Evaluate for Plasmodium parasites.
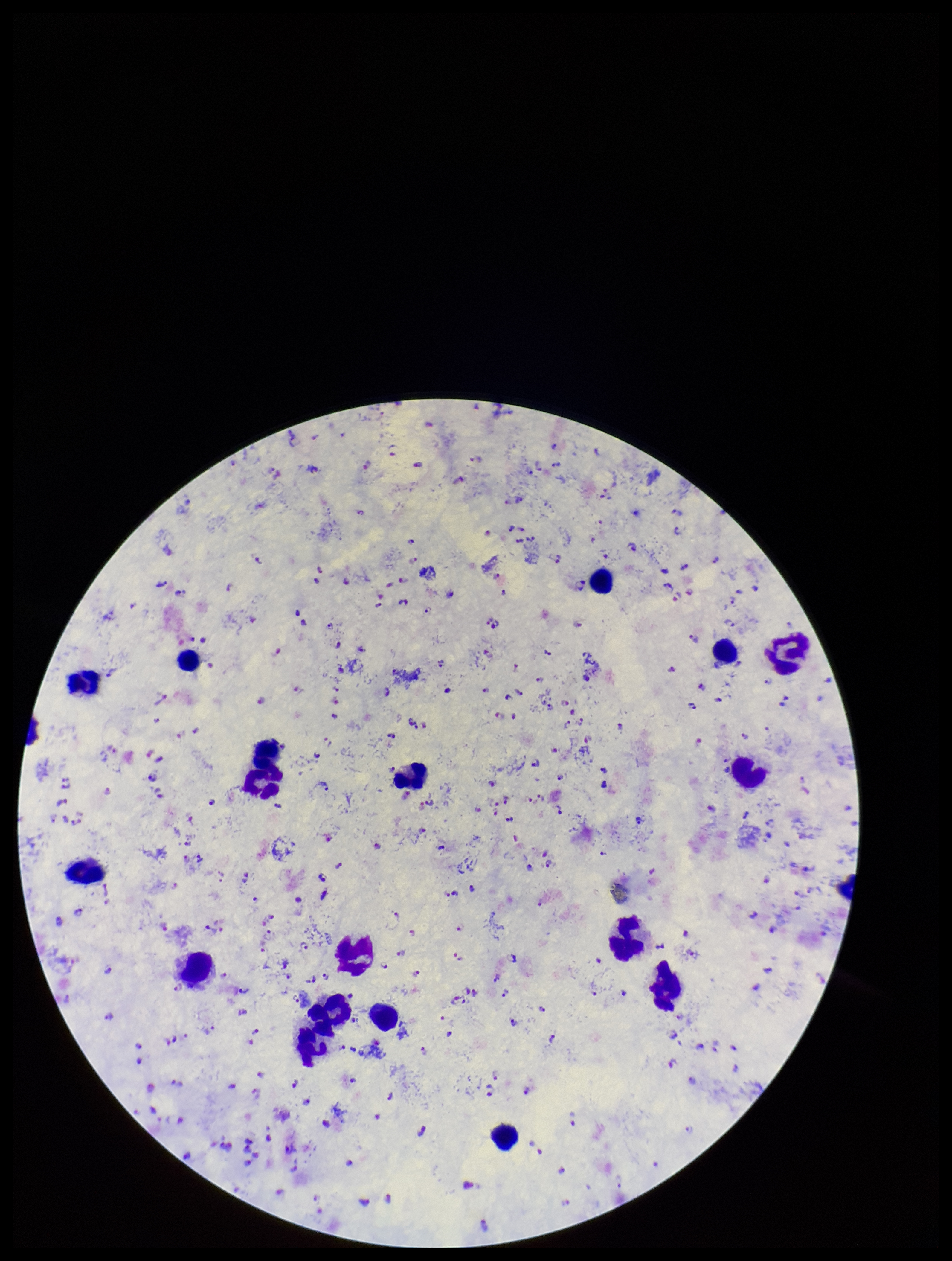
Detected.

image size = 952×1261 pixels
leukocyte count = 18
preparation = thick smear
field of view = one from this slide
capture = smartphone photograph through the microscope eyepiece
stain = Giemsa
parasite count = 230
species reported for this patient = Plasmodium falciparum
patient malaria status = infected